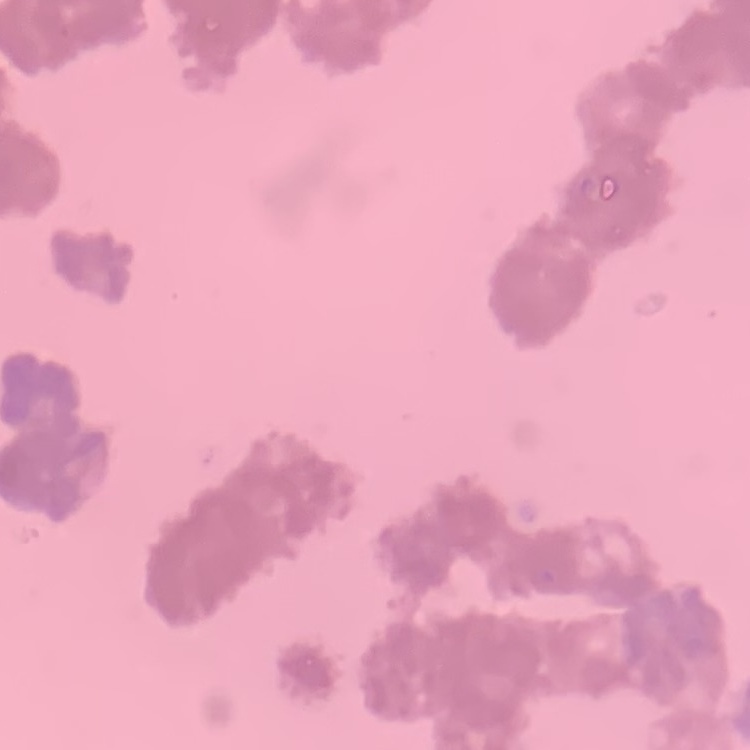

red blood cell morphology = rouleaux formation
preparation = thin blood film
image type = one tile cut from a larger photomicrograph
stain = Field's or Giemsa